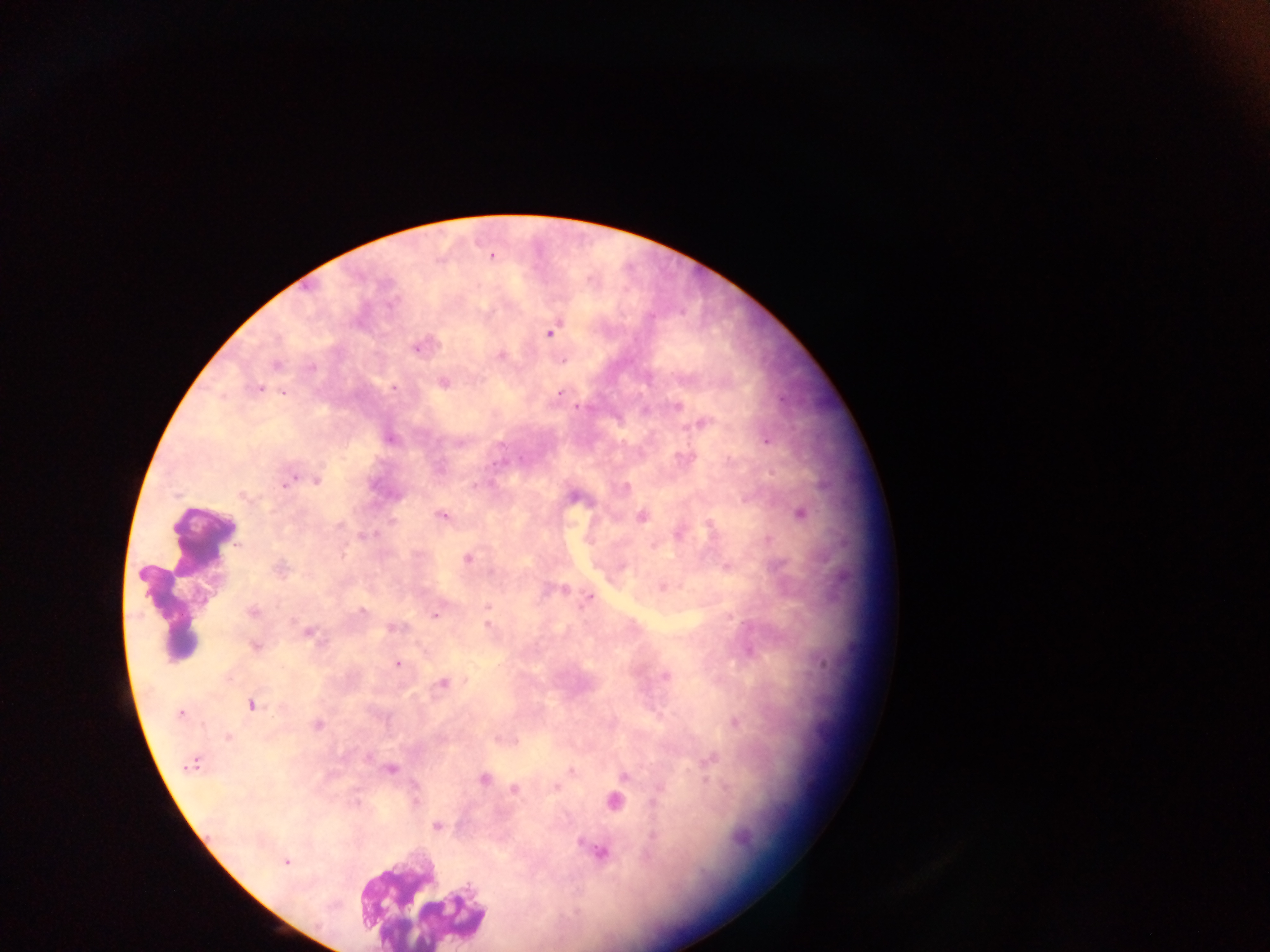
{
  "malaria_parasite_locations": "approximate centers as x y in pixels: 492 257; 550 332; 416 348; 500 356; 275 365; 444 383; 394 388; 258 389; 283 393; 559 393; 577 406; 677 406; 703 422; 390 439; 766 441; 458 444; 316 481; 286 482; 475 485; 243 496; 573 497; 800 514; 442 516; 642 516; 393 521; 365 536; 767 539; 467 558; 279 570; 663 587; 565 589; 590 597; 488 606; 253 611; 363 611; 435 615; 488 625; 393 627; 307 633; 256 647; 398 664; 665 676; 442 684; 251 705; 179 714; 735 722; 317 725; 228 737; 368 759; 710 760; 191 763; 390 770; 572 771; 624 776; 483 779; 556 787; 514 789; 653 801; 614 802; 357 803; 437 827; 601 852; 286 862",
  "country": "Ghana",
  "field_of_view": "single",
  "leukocyte_locations": "approximate centers as x y in pixels: 203 535; 168 604; 418 902",
  "preparation": "thick blood smear",
  "capture": "mobile-phone photograph through a microscope",
  "image_size": "1270×952 pixels"
}